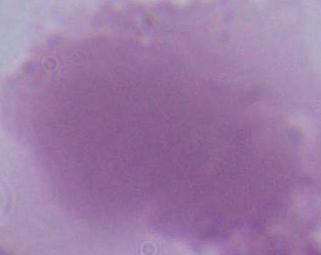
modality = micrograph
identification = erythrocyte
magnification = 1000x